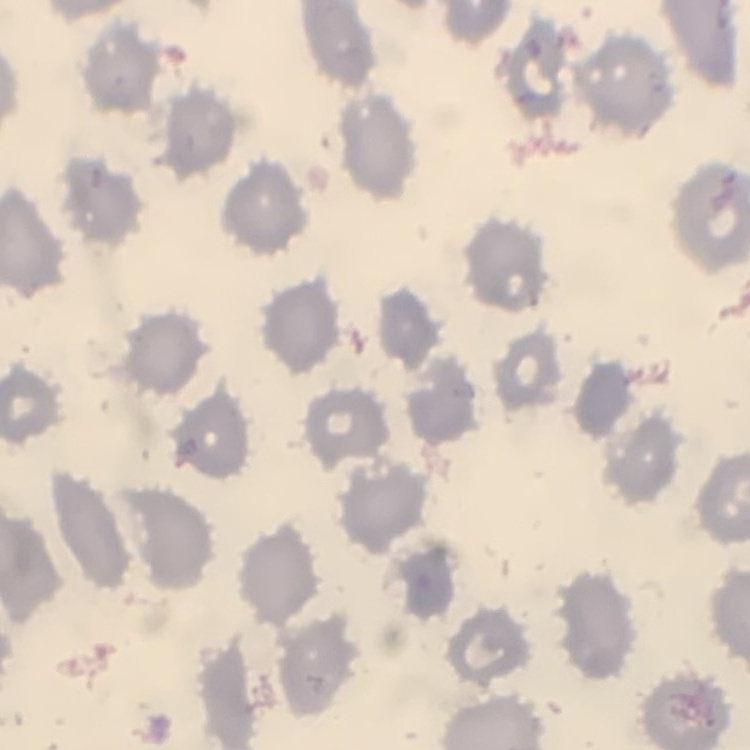
The red blood cells show no rouleaux formation. Stained with either Field's or Giemsa. Thin blood film. One tile cut from a larger photomicrograph.